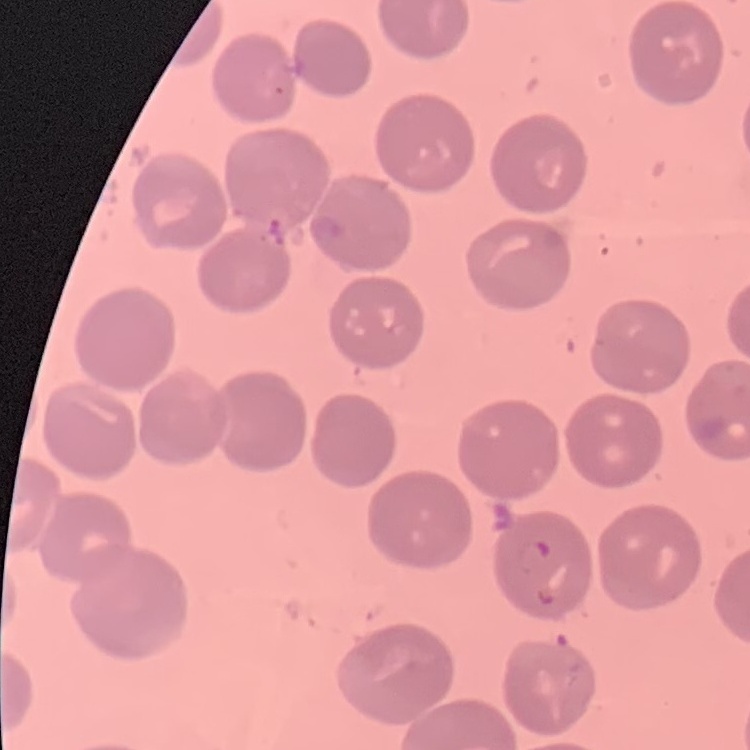
Summary:
  - Red blood cell morphology: no rouleaux formation
  - Stain: Field's or Giemsa
  - Preparation: thin blood film
  - Image type: square crop of a larger photomicrograph